Identify the preparation type.
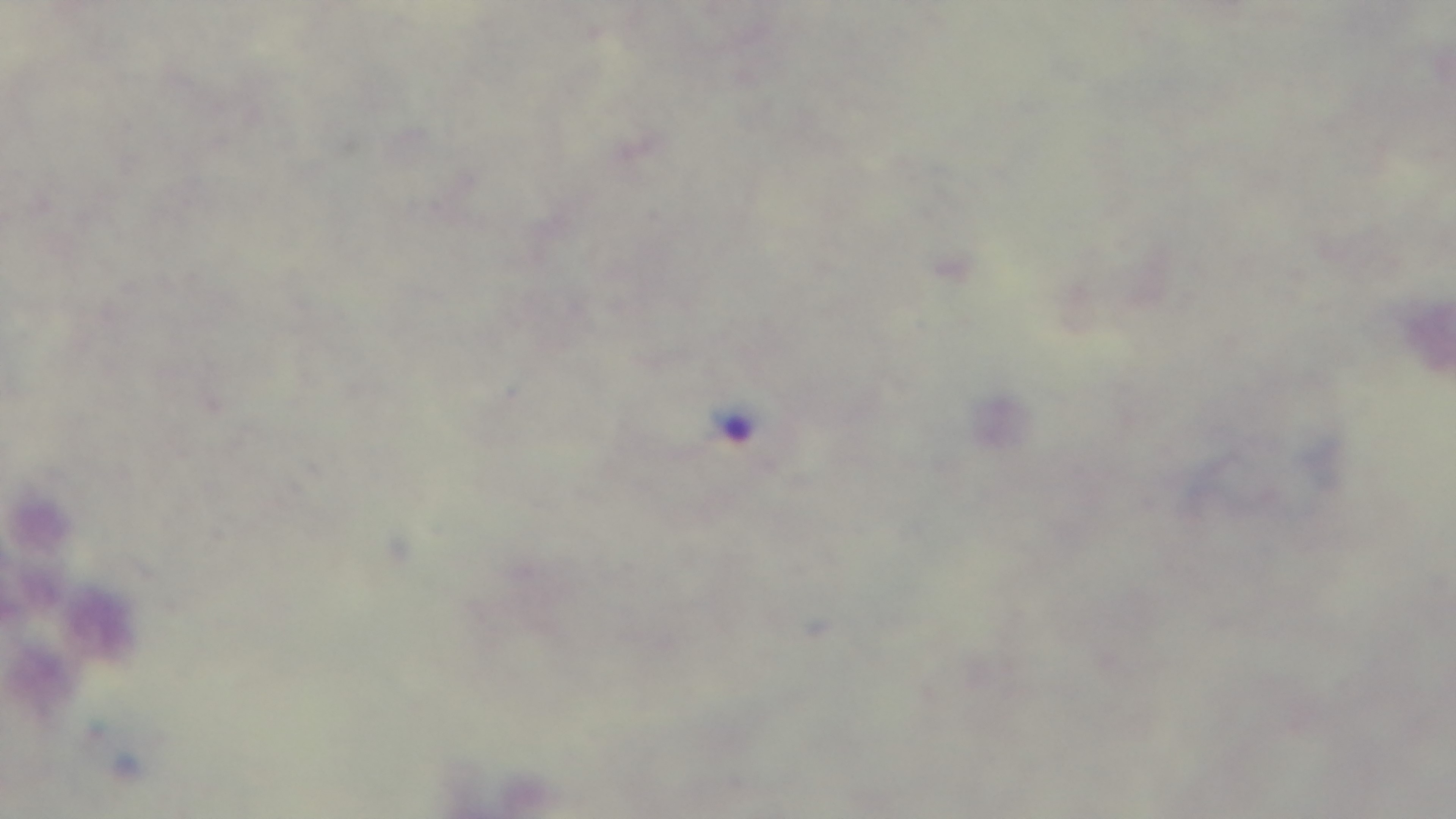

Thick.

Summary:
  - Stain: Giemsa
  - Objective: 100x oil immersion
  - Malaria status: positive
  - Capture: mounted 4K digital camera
  - Modality: light microscopy
  - Field of view: single